Name the cell type shown.
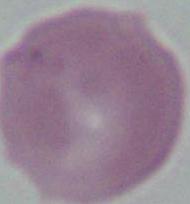

This is an erythrocyte.

Summary:
  - Magnification: 1000x
  - Modality: photomicrograph